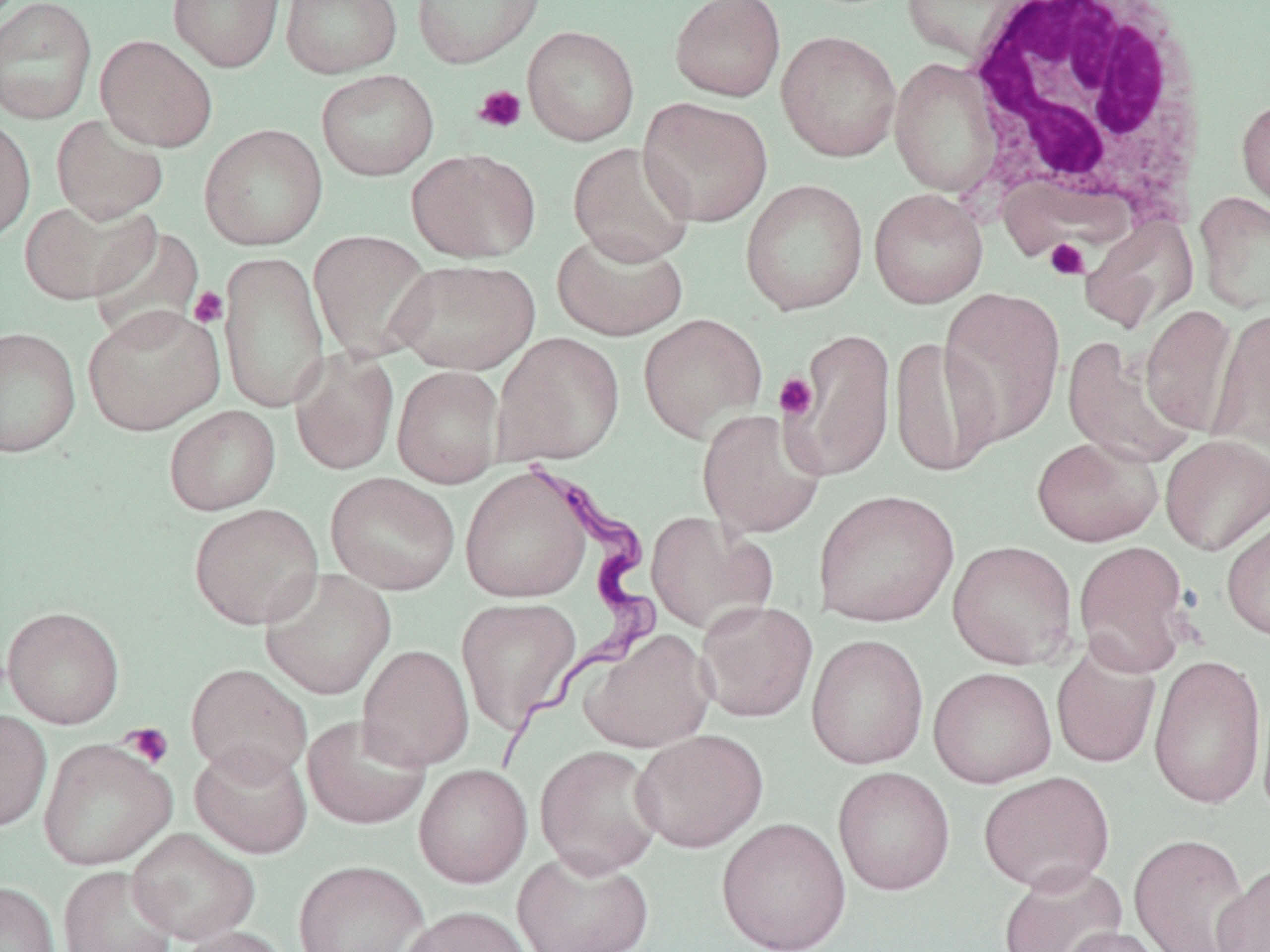

{
  "slide_level_diagnosis": "Trypanosoma brucei",
  "stain": "May-Grünwald-Giemsa",
  "magnification": "1000x",
  "modality": "optical microscopy",
  "image_size": "1270×952 pixels",
  "field_of_view": "single",
  "white_blood_cell_locations": "approximate bounding boxes as (x1, y1, x2, y2) in pixels: (961, 0, 1212, 226)",
  "preparation": "thin blood smear",
  "trypanosoma_brucei_locations": "approximate bounding boxes as (x1, y1, x2, y2) in pixels: (492, 451, 663, 778)",
  "platelet_locations": "approximate bounding boxes as (x1, y1, x2, y2) in pixels: (473, 85, 527, 133), (1044, 238, 1090, 280), (188, 286, 229, 328), (774, 372, 818, 421), (122, 723, 174, 768)",
  "uninfected_red_blood_cell_locations": "approximate bounding boxes as (x1, y1, x2, y2) in pixels: (0, 0, 97, 124), (167, 0, 285, 72), (280, 0, 402, 78), (410, 0, 545, 69), (668, 0, 787, 102), (901, 0, 1036, 64), (522, 25, 640, 146), (775, 30, 902, 162), (96, 34, 217, 152), (889, 58, 1002, 197), (316, 69, 439, 181), (1235, 93, 1270, 218), (637, 97, 773, 227), (0, 114, 36, 245), (51, 114, 169, 225), (199, 124, 328, 251), (567, 142, 696, 267), (406, 148, 541, 263), (740, 178, 869, 316), (868, 188, 988, 308), (1194, 191, 1270, 313), (19, 197, 158, 305), (1078, 213, 1199, 334), (89, 225, 207, 346), (551, 229, 688, 341), (308, 230, 437, 362), (218, 250, 330, 412), (389, 259, 540, 375), (938, 287, 1066, 447), (83, 303, 225, 435), (1140, 303, 1240, 437), (1207, 309, 1270, 451), (637, 313, 768, 441), (0, 326, 80, 458), (786, 328, 896, 481), (492, 332, 625, 465), (889, 335, 1000, 479), (1061, 337, 1197, 469), (289, 346, 400, 476), (391, 365, 505, 487), (164, 404, 281, 515), (696, 408, 827, 539), (1160, 434, 1270, 555), (1031, 435, 1164, 547), (459, 465, 593, 603), (325, 472, 460, 595), (812, 488, 959, 628), (189, 502, 324, 630), (645, 511, 776, 636), (1221, 514, 1270, 643), (947, 540, 1079, 670), (1073, 540, 1192, 677), (259, 568, 396, 700), (456, 597, 581, 734), (695, 600, 818, 723), (2, 605, 125, 729), (581, 629, 715, 753), (806, 634, 929, 769), (357, 644, 474, 771), (1051, 644, 1161, 768), (1149, 653, 1267, 811), (185, 663, 312, 782), (927, 666, 1057, 788), (1256, 679, 1270, 825), (0, 709, 52, 832), (302, 714, 431, 830), (631, 728, 768, 853), (38, 738, 177, 871), (189, 741, 313, 858), (534, 744, 665, 878), (414, 764, 532, 888), (832, 766, 955, 896), (978, 771, 1116, 894), (716, 817, 851, 952), (126, 827, 260, 945), (1127, 832, 1253, 951), (512, 848, 655, 952), (293, 860, 429, 952), (1213, 861, 1269, 952), (998, 862, 1127, 952), (57, 865, 179, 952), (0, 881, 60, 952), (399, 906, 535, 952), (1058, 925, 1173, 952), (173, 926, 291, 952)"
}